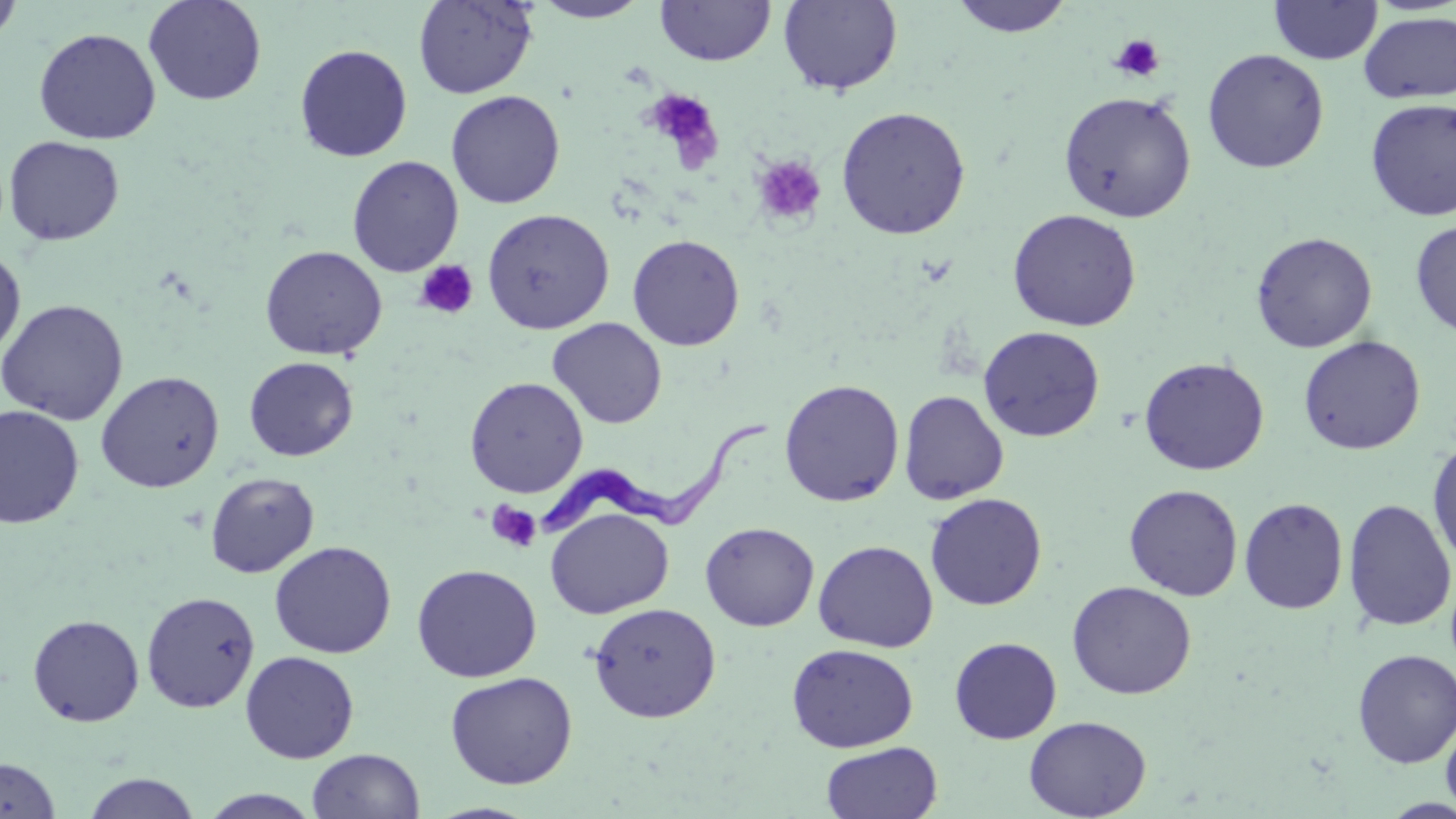 Approximate bounding boxes as [x1, y1, x2, y2] in pixels. Trypanosoma brucei locations: [532, 417, 772, 538]. Uninfected red blood cell locations: [0, 0, 22, 50], [144, 0, 267, 105], [413, 0, 537, 99], [530, 0, 651, 23], [655, 0, 775, 66], [778, 0, 903, 96], [948, 0, 1076, 38], [1269, 0, 1382, 65], [1358, 11, 1456, 104], [33, 27, 161, 144], [294, 44, 412, 162], [1202, 48, 1329, 173], [446, 90, 565, 209], [1058, 91, 1196, 222], [1364, 98, 1456, 221], [836, 105, 971, 240], [3, 135, 125, 246], [347, 155, 464, 277], [481, 208, 615, 333], [1007, 208, 1142, 332], [1410, 220, 1456, 339], [1251, 231, 1378, 353], [627, 234, 745, 350], [0, 245, 26, 362], [259, 245, 387, 360], [0, 299, 128, 425], [547, 318, 667, 429], [978, 326, 1105, 442], [1298, 335, 1426, 455], [244, 356, 358, 461], [1138, 356, 1270, 475], [95, 371, 224, 493], [464, 376, 588, 498], [778, 379, 905, 507], [899, 390, 1009, 505], [0, 405, 84, 529], [1427, 436, 1456, 572], [205, 471, 319, 578], [1124, 484, 1243, 601], [925, 492, 1047, 611], [1239, 497, 1348, 614], [1342, 499, 1455, 632], [545, 507, 674, 619], [700, 522, 819, 631], [813, 540, 938, 652], [269, 541, 396, 659], [411, 563, 542, 682], [1067, 580, 1197, 700], [141, 590, 260, 713], [588, 602, 722, 723], [27, 614, 145, 727], [950, 637, 1062, 744], [786, 643, 919, 752], [1352, 649, 1456, 768], [240, 650, 359, 763], [445, 671, 578, 789], [1440, 712, 1456, 818], [1024, 715, 1151, 819], [821, 742, 943, 819], [307, 748, 425, 819], [0, 757, 61, 818], [81, 772, 202, 818], [199, 789, 323, 818]. Platelet locations: [1109, 33, 1166, 82], [642, 88, 724, 170], [752, 154, 827, 227], [415, 260, 478, 320], [486, 501, 542, 553]. Slide-level diagnosis: Trypanosoma brucei. May-Grünwald-Giemsa-stained preparation. Optical microscopy. Image is 1456×819 pixels. 1000x magnification. One field of a larger specimen. Thin blood smear.